Name the parasite shown.
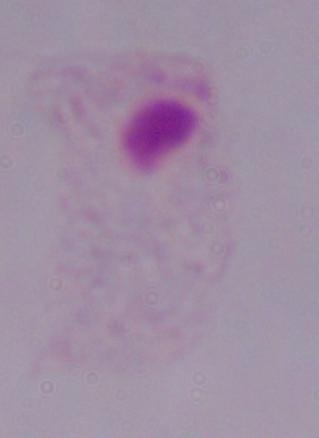

A trichomonad.

{
  "modality": "photomicrograph",
  "magnification": "1000x"
}